Report the malaria status of this cell.
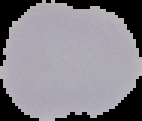
It is uninfected.

image type = cell region segmented out of the field of view; surrounding area masked to black
preparation = thin blood smear
image size = 142×121 pixels